Locate every Plasmodium parasite.
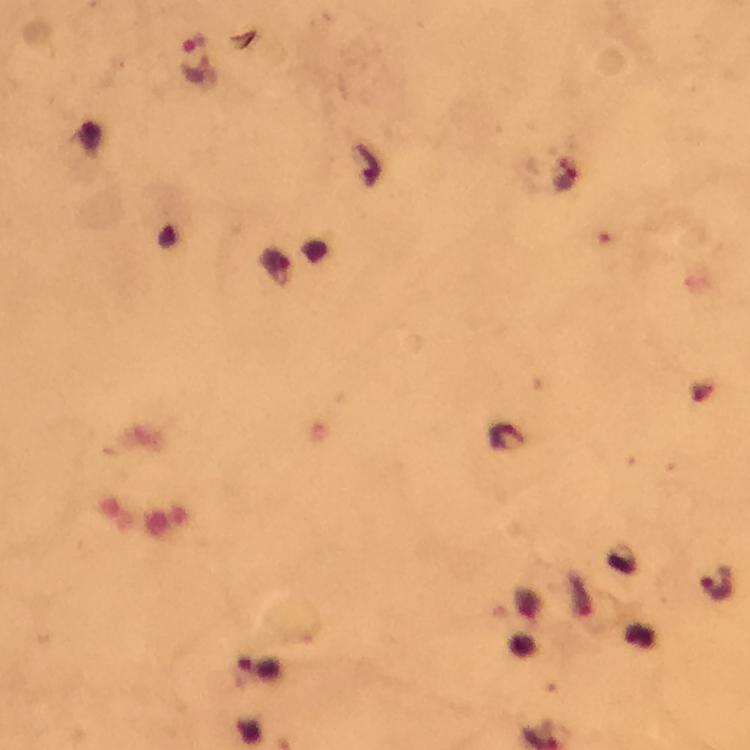
Approximate object centers, in pixels from the top-left corner.
Plasmodium parasites: (x=193, y=62), (x=717, y=584).

Summary:
  - Image size: 750×750 pixels
  - Magnification: 100x
  - Immersion oil: used
  - Preparation: thick blood film
  - Capture: smartphone photograph through a microscope
  - Context: from a diagnostic examination for malaria
  - Stain: Giemsa
  - Cropped from: a single field of view